Outline platelets.
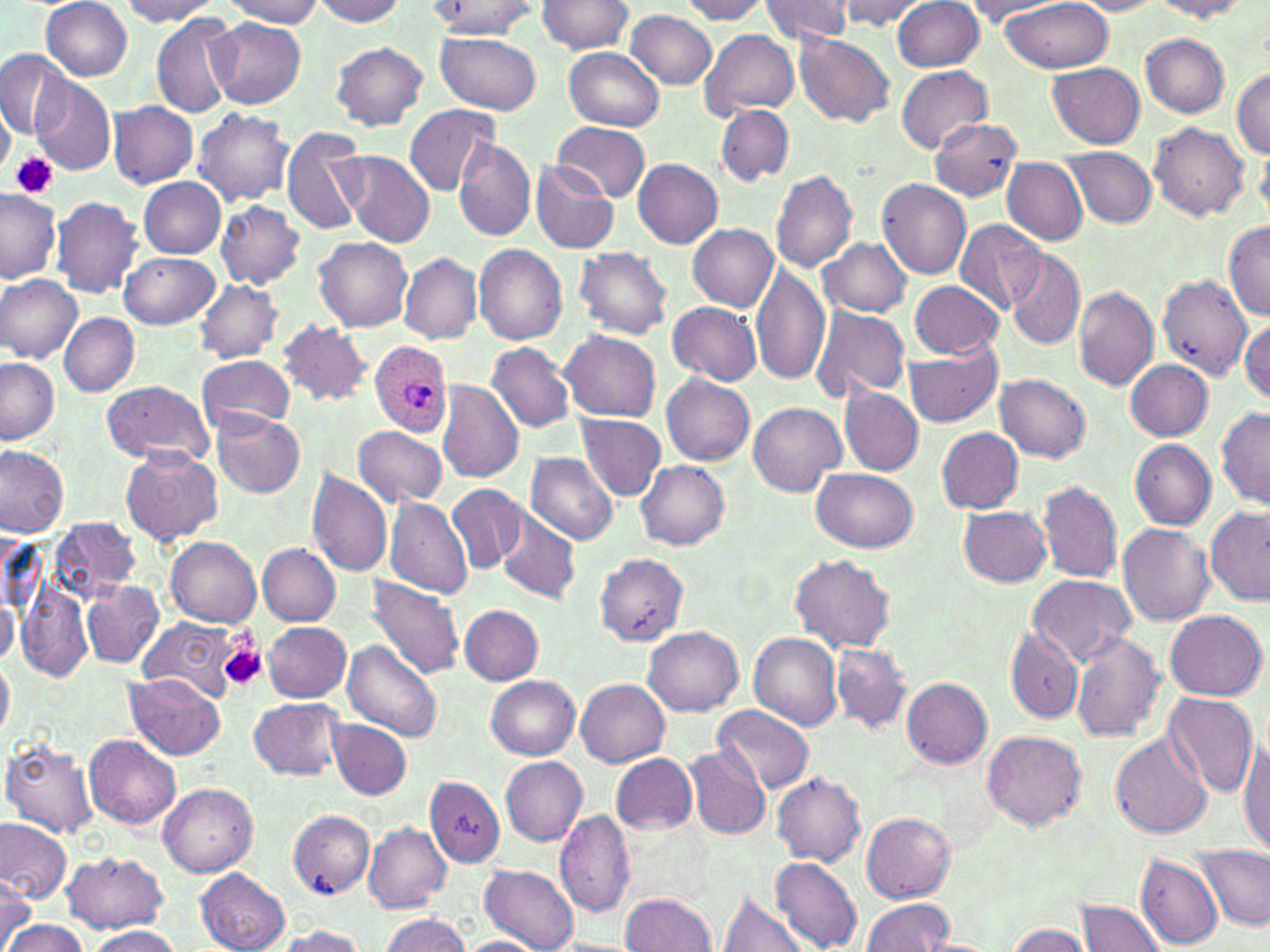

Approximate bounding boxes as (x1, y1, x2, y2) in pixels.
Platelets: (11, 153, 60, 200), (220, 644, 267, 692).

Plasmodium ovale-infected red blood cell locations: (371, 341, 453, 438). Uninfected red blood cell locations: (120, 0, 219, 25), (225, 0, 326, 27), (311, 0, 406, 25), (677, 0, 770, 23), (757, 0, 853, 43), (836, 0, 924, 30), (892, 0, 984, 72), (1154, 0, 1252, 19), (42, 1, 134, 80), (966, 1, 1068, 20), (1002, 1, 1112, 73), (1070, 1, 1167, 15), (425, 2, 541, 39), (535, 2, 635, 55), (626, 9, 718, 90), (151, 12, 239, 120), (210, 17, 306, 108), (700, 28, 800, 120), (435, 32, 540, 115), (794, 32, 894, 127), (1141, 33, 1229, 117), (330, 42, 428, 131), (562, 48, 665, 131), (0, 50, 72, 139), (1049, 64, 1144, 148), (896, 66, 994, 152), (1232, 69, 1270, 158), (31, 78, 116, 176), (109, 101, 198, 188), (0, 103, 14, 178), (405, 104, 499, 197), (716, 104, 794, 185), (192, 109, 295, 207), (927, 119, 1021, 199), (1150, 120, 1249, 221), (552, 123, 650, 202), (281, 126, 370, 238), (454, 140, 536, 244), (1257, 144, 1270, 219), (1063, 147, 1157, 227), (340, 152, 436, 248), (632, 158, 723, 248), (1003, 159, 1087, 244), (530, 160, 619, 254), (770, 169, 858, 273), (138, 178, 226, 258), (877, 179, 972, 279), (0, 191, 60, 281), (49, 195, 146, 298), (215, 201, 306, 290), (955, 219, 1047, 313), (688, 222, 779, 311), (1221, 222, 1270, 319), (313, 238, 413, 332), (820, 238, 911, 318), (473, 244, 568, 345), (574, 247, 673, 339), (1006, 249, 1085, 349), (399, 251, 482, 343), (119, 253, 219, 329), (751, 261, 830, 387), (1157, 273, 1253, 379), (0, 275, 83, 364), (195, 279, 283, 362), (907, 281, 1004, 358), (1073, 286, 1159, 391), (667, 302, 762, 385), (809, 308, 910, 399), (60, 313, 140, 396), (1239, 318, 1270, 403), (276, 319, 374, 406), (559, 330, 661, 421), (487, 342, 575, 433), (905, 346, 1002, 428), (197, 355, 295, 435), (0, 358, 59, 446), (1125, 359, 1212, 441), (660, 372, 755, 466), (996, 374, 1091, 461), (100, 379, 216, 465), (436, 380, 525, 485), (841, 387, 924, 476), (747, 402, 846, 496), (1216, 407, 1269, 509), (212, 411, 305, 499), (577, 414, 666, 500), (353, 425, 447, 507), (936, 427, 1023, 514), (1128, 439, 1217, 530), (0, 445, 69, 537), (121, 449, 223, 546), (525, 452, 619, 544), (636, 462, 730, 550), (308, 468, 394, 578), (811, 469, 921, 552), (1038, 481, 1123, 582), (447, 483, 527, 573), (384, 497, 474, 597), (1205, 504, 1270, 608), (959, 506, 1052, 587), (498, 510, 580, 604), (52, 518, 139, 601), (1118, 523, 1215, 628), (167, 537, 261, 625), (258, 543, 339, 624), (593, 552, 687, 645), (788, 554, 896, 652), (1026, 574, 1137, 666), (365, 575, 467, 681), (17, 578, 94, 681), (82, 580, 163, 669), (0, 598, 19, 664), (460, 605, 543, 684), (1165, 610, 1268, 700), (139, 617, 241, 704), (262, 621, 350, 701), (643, 626, 743, 716), (1003, 626, 1085, 723), (749, 632, 844, 729), (1071, 633, 1165, 741), (344, 640, 441, 743), (830, 643, 911, 733), (0, 659, 14, 741), (125, 674, 223, 760), (487, 676, 580, 759), (576, 678, 671, 766), (901, 678, 992, 769), (1162, 692, 1259, 800), (248, 696, 346, 780), (713, 705, 814, 794), (330, 719, 411, 799), (980, 729, 1088, 832), (1110, 733, 1214, 839), (84, 734, 181, 831), (2, 739, 100, 837), (1237, 741, 1270, 857), (684, 747, 771, 841), (611, 753, 698, 834), (501, 756, 589, 846), (771, 772, 866, 866), (427, 776, 506, 868), (159, 782, 258, 877), (553, 810, 636, 920), (288, 811, 374, 898), (862, 813, 955, 901), (0, 819, 72, 904), (364, 822, 451, 913), (1189, 844, 1270, 931), (62, 850, 169, 934), (1134, 851, 1225, 950), (771, 857, 862, 952), (481, 865, 580, 952), (196, 868, 290, 952), (0, 872, 35, 950), (718, 890, 812, 952), (621, 892, 716, 951), (862, 897, 955, 950), (1075, 898, 1169, 952), (380, 913, 471, 952), (0, 917, 84, 952), (1002, 923, 1096, 952), (272, 925, 366, 952), (87, 926, 184, 952), (456, 936, 545, 952), (545, 938, 646, 952). Slide-level diagnosis: Plasmodium ovale. Optical microscopy. Image is 1270×952 pixels. Single field of view. 1000x magnification. Thin blood smear. May-Grünwald-Giemsa-stained preparation.